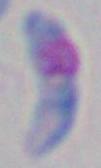
Summary:
  - Magnification: 1000x
  - Modality: micrograph
  - Identification: Toxoplasma gondii